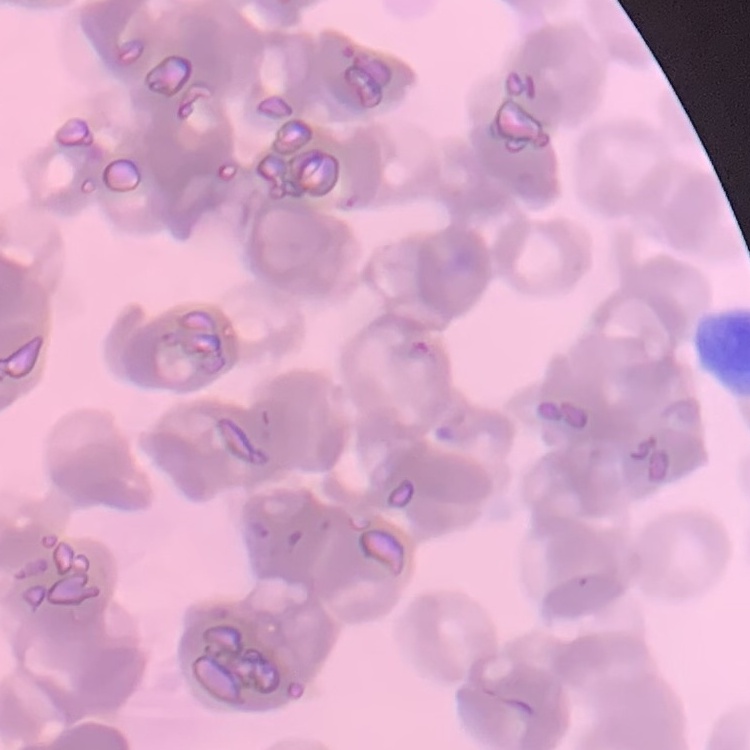

The erythrocytes show rouleaux formation. Stained with either Field's or Giemsa. Thin blood smear. Square crop of a larger photomicrograph.